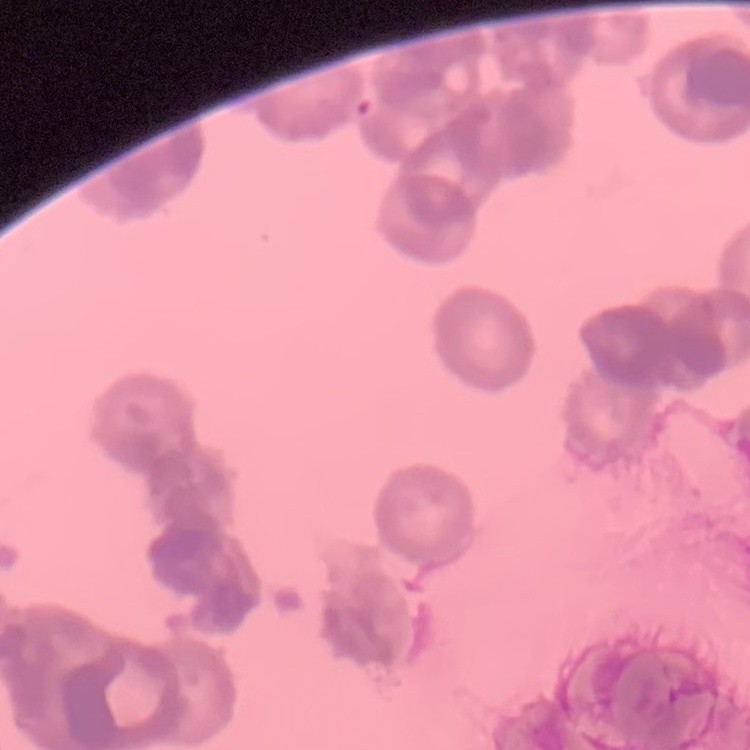 The erythrocytes exhibit rouleaux formation. Stained with either Field's or Giemsa. Square crop of a larger photomicrograph. Thin blood smear.